Point out each malaria parasite.
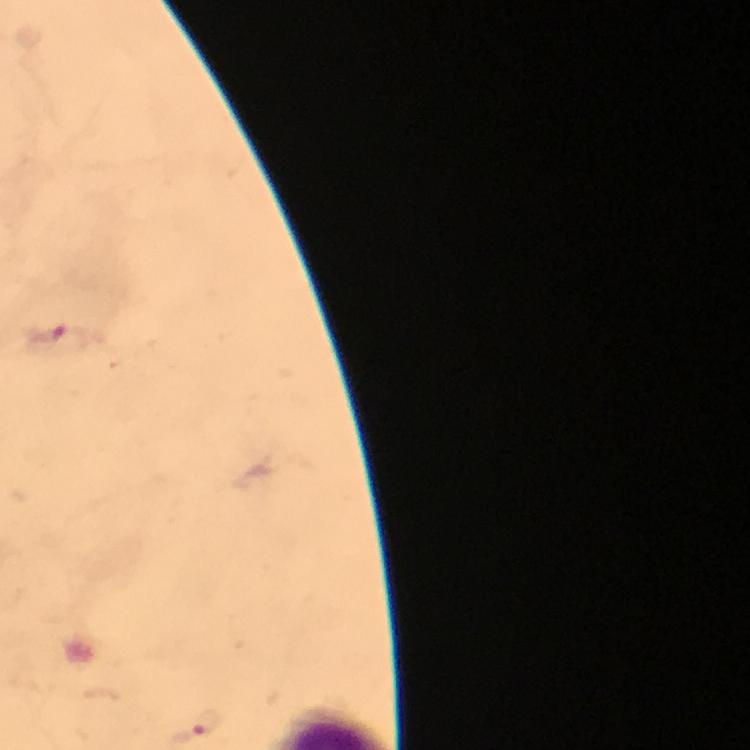
Approximate centers as (x, y) in pixels.
Malaria parasites: (68, 341), (208, 724).

Summary:
  - Context: from a diagnostic examination for malaria
  - Magnification: 100x
  - Cropped from: one field of view
  - Capture: smartphone photograph through a microscope
  - Immersion oil: applied
  - Preparation: thick blood smear
  - Image size: 750×750 pixels
  - Stain: Giemsa